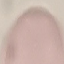
Summary:
  - Malaria status: uninfected
  - Capture: smartphone camera at the microscope eyepiece
  - Preparation: thin blood film
  - Stain: Giemsa
  - Image type: cell patch, automatically extracted from a larger field of view and resized to 64 × 64 pixels